Comment on the morphology of the red blood cells.
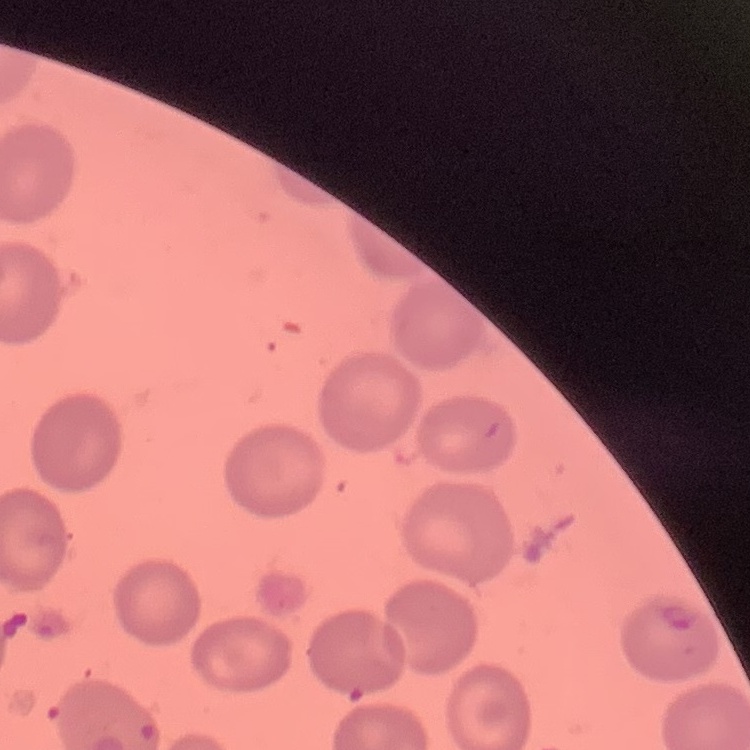

No rouleaux formation.

Summary:
  - Image type: one tile cut from a larger photomicrograph
  - Stain: Field's or Giemsa
  - Preparation: thin blood smear